Assess this cell for malaria.
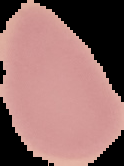
It is uninfected.

image type = cell region segmented out of the field of view; surrounding area masked to black
preparation = thin blood smear
image size = 124×166 pixels